State which cell type is depicted.
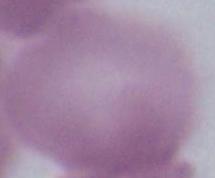

This is an erythrocyte.

Summary:
  - Modality: micrograph
  - Magnification: 1000x